Locate and identify every blood parasite.
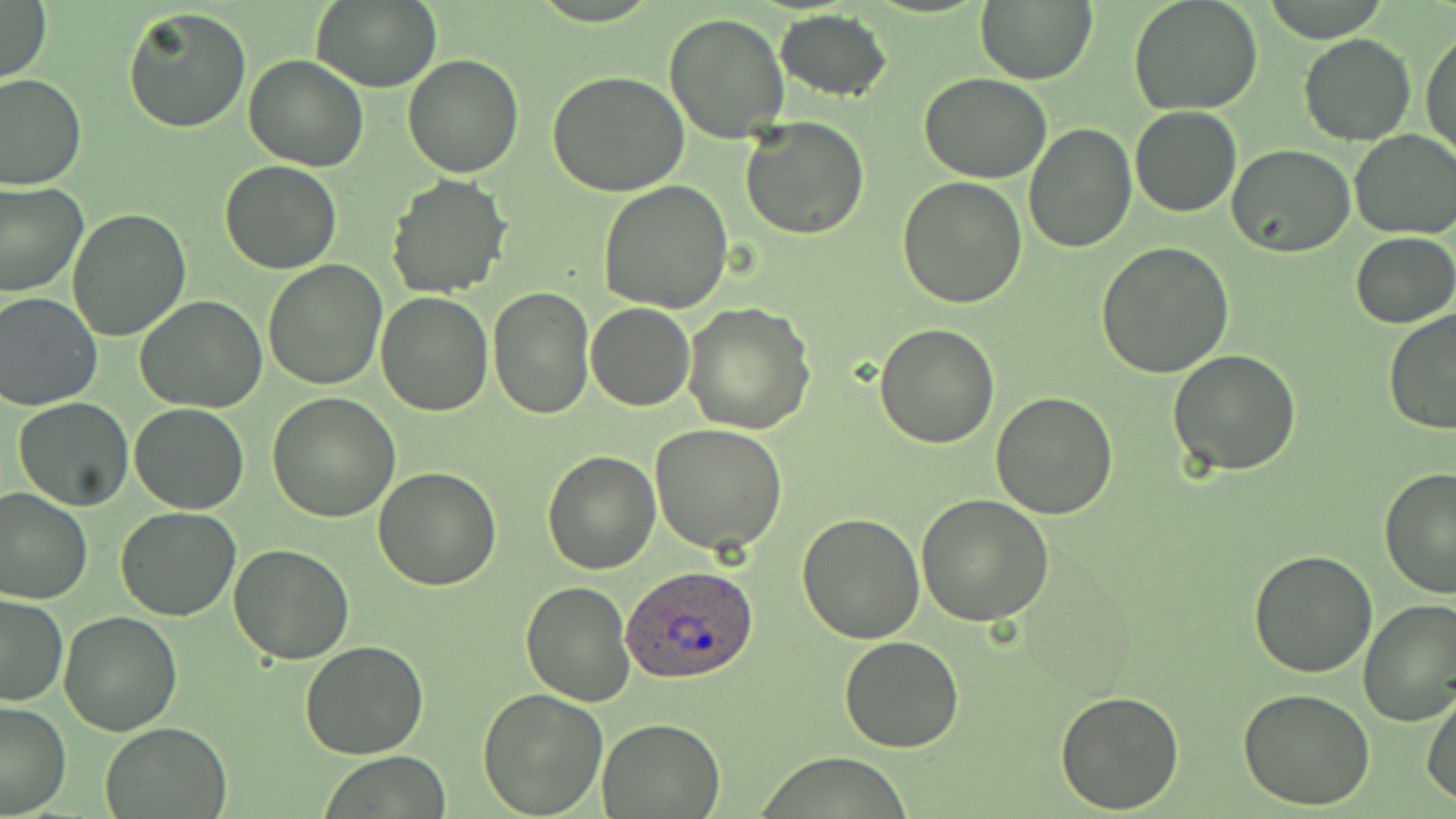

Approximate bounding boxes as (x1,y1)-(x2,y2) corner pairs in pixels.
Plasmodium ovale-infected red blood cells: (621,562)-(761,684).
No Plasmodium falciparum, Plasmodium malariae, Plasmodium vivax, Babesia divergens, or Trypanosoma brucei observed.

slide-level diagnosis = Plasmodium ovale
field of view = one of a larger specimen
magnification = 1000x
image size = 1456×819 pixels
uninfected red blood cell locations = approximate bounding boxes as (x1,y1)-(x2,y2) corner pairs in pixels: (311,0)-(441,93), (1129,0)-(1265,116), (0,1)-(50,85), (975,1)-(1098,84), (122,7)-(253,134), (774,8)-(893,103), (663,13)-(789,143), (1421,25)-(1455,163), (1298,33)-(1416,147), (403,53)-(525,177), (242,55)-(368,172), (547,70)-(690,196), (0,73)-(86,190), (920,73)-(1053,183), (1130,106)-(1243,217), (739,115)-(870,240), (1023,123)-(1136,254), (1349,129)-(1456,239), (1227,145)-(1355,258), (220,160)-(342,275), (387,174)-(513,297), (897,175)-(1027,308), (0,180)-(88,298), (599,181)-(734,315), (67,208)-(194,340), (1351,232)-(1456,329), (1095,240)-(1234,379), (262,259)-(387,391), (488,285)-(594,417), (0,291)-(102,411), (375,292)-(494,416), (134,295)-(266,413), (586,302)-(695,411), (683,302)-(816,433), (1382,308)-(1456,436), (874,322)-(1000,447), (1167,349)-(1302,478), (989,391)-(1118,520), (268,393)-(399,522), (12,398)-(134,512), (129,403)-(250,515), (649,423)-(787,555), (542,449)-(661,574), (1378,466)-(1456,598), (372,467)-(502,590), (0,487)-(92,606), (916,493)-(1055,627), (115,506)-(240,621), (796,514)-(925,644), (228,544)-(354,663), (1248,549)-(1379,678), (520,578)-(636,705), (0,594)-(69,706), (1357,598)-(1456,727), (59,611)-(182,735), (839,635)-(965,753), (299,640)-(429,760), (476,686)-(606,816), (1055,687)-(1185,812), (1238,690)-(1376,811), (1422,690)-(1456,805), (0,701)-(71,817), (597,717)-(724,816), (101,720)-(232,817), (322,752)-(451,817)
stain = May-Grünwald-Giemsa
modality = optical microscopy
preparation = thin blood film